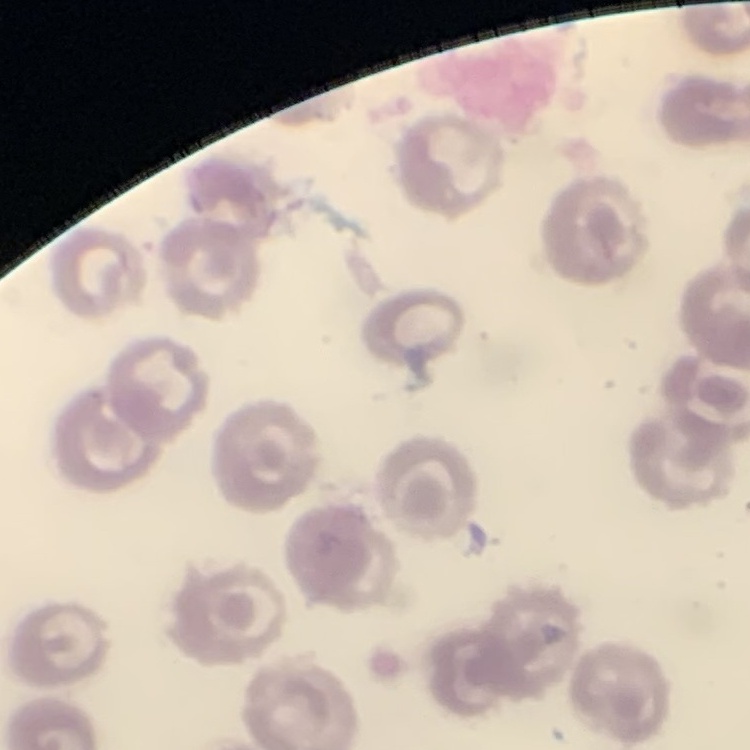

erythrocyte morphology = no rouleaux formation
stain = Field's or Giemsa
image type = one tile cut from a larger photomicrograph
preparation = thin blood film